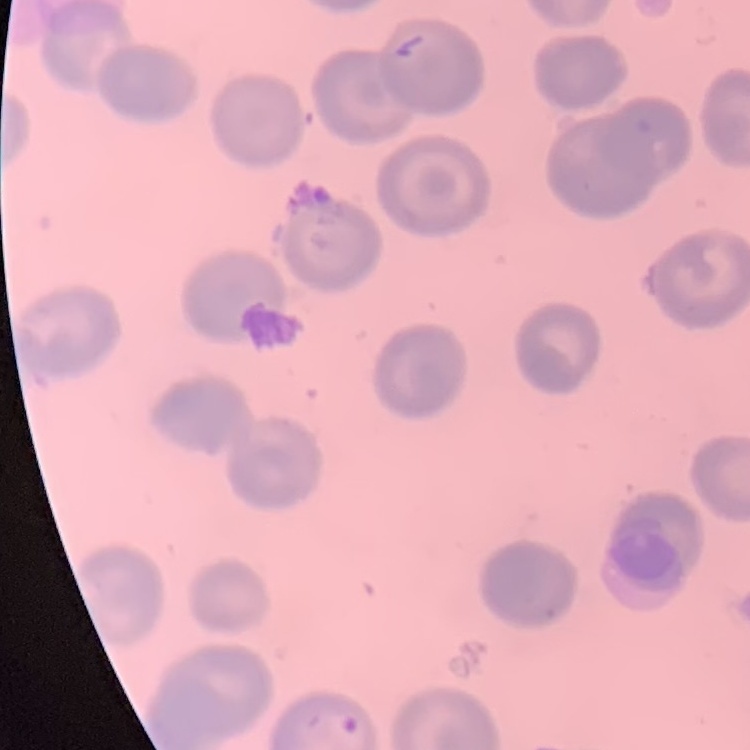
The erythrocytes exhibit no rouleaux formation. Stained with either Field's or Giemsa. Thin blood smear. One tile cut from a larger photomicrograph.